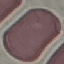 Malaria status: uninfected. Giemsa stain. Automatically extracted cell patch, resized to 64 × 64 pixels. Thin smear of blood. Photographed with a smartphone camera at the microscope eyepiece.